Name the cell type shown.
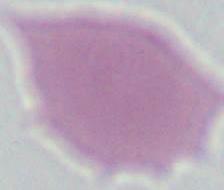
An erythrocyte.

modality: photomicrograph
magnification: 1000x